Classify this cell by malaria status.
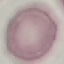

It is uninfected.

Cell patch, automatically extracted from a larger field of view and resized to 64 × 64 pixels. Giemsa-stained preparation. Thin smear of blood. Acquired by smartphone through the microscope eyepiece.